Identify the parasite.
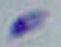
This is Toxoplasma gondii.

Photomicrograph. Captured at 1000x magnification.